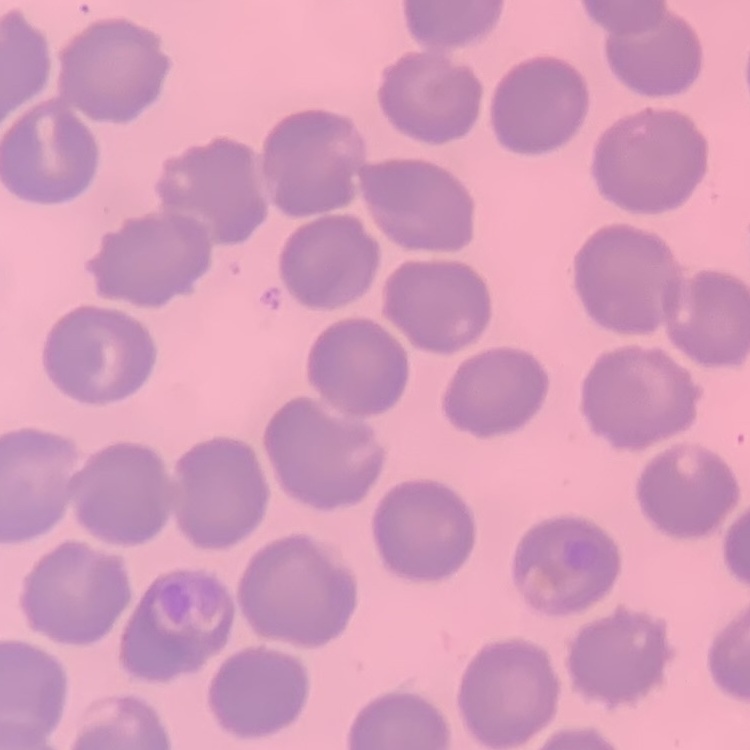

erythrocyte morphology = no rouleaux formation
preparation = thin peripheral smear
stain = Field's or Giemsa
image type = one tile cut from a larger photomicrograph